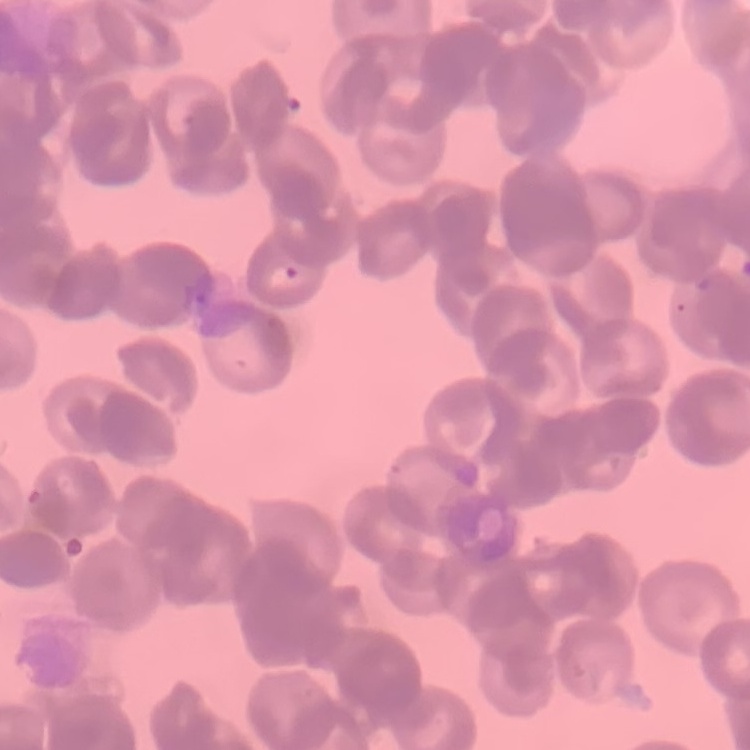 The erythrocytes exhibit rouleaux formation. Thin blood smear. One tile cut from a larger photomicrograph. Field's or Giemsa stain.